Identify the parasite.
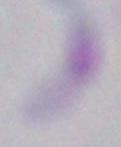

Toxoplasma gondii.

{
  "magnification": "1000x",
  "modality": "micrograph"
}